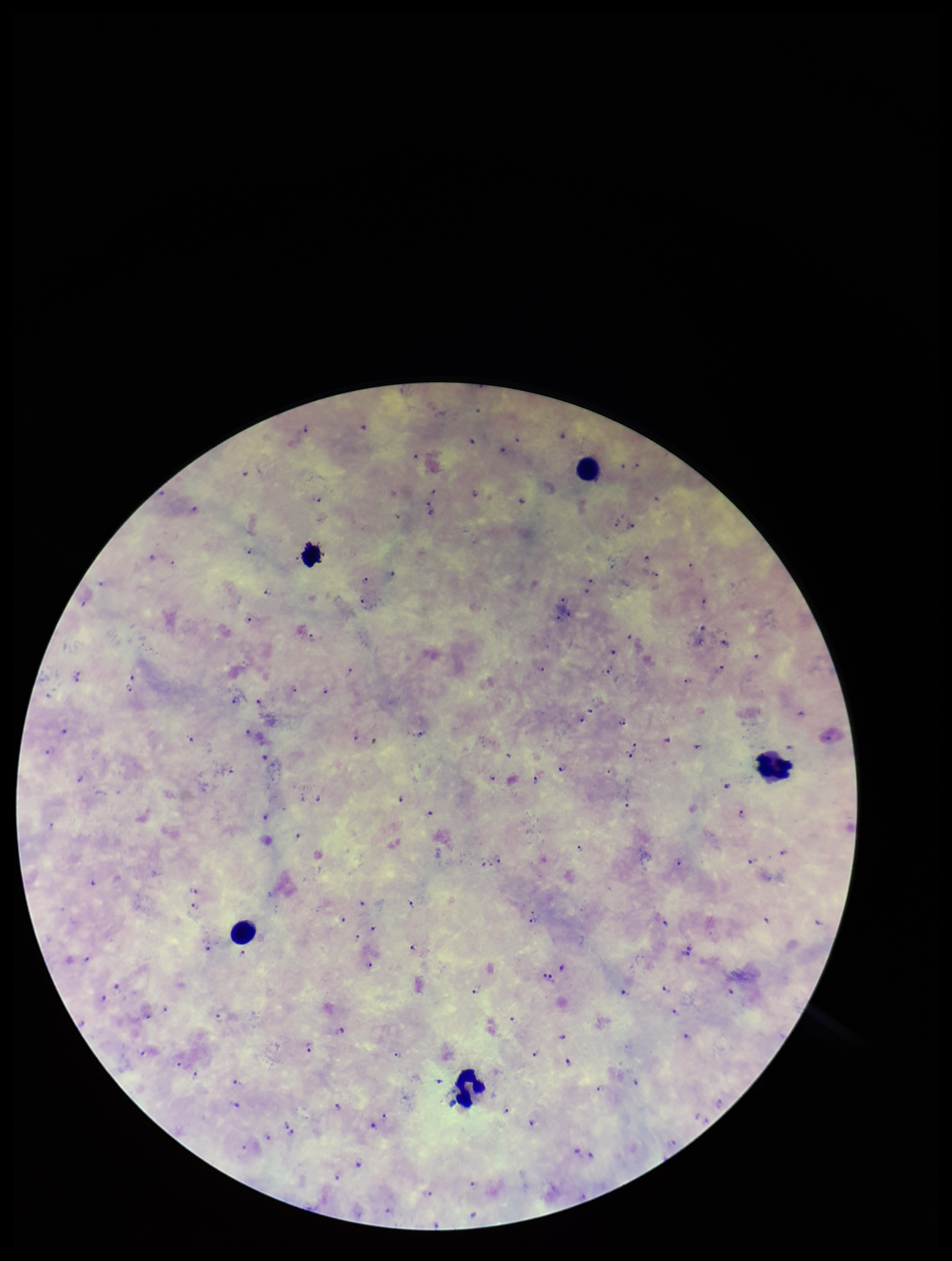
Image is 952×1261 pixels. Plasmodium parasites: seen. Leukocyte count: 5. One field from this slide. Patient malaria status: infected. Preparation: thick smear. Giemsa stain. Smartphone photograph taken through the eyepiece of a microscope. Parasite count: 133. Species reported for this patient: Plasmodium falciparum.